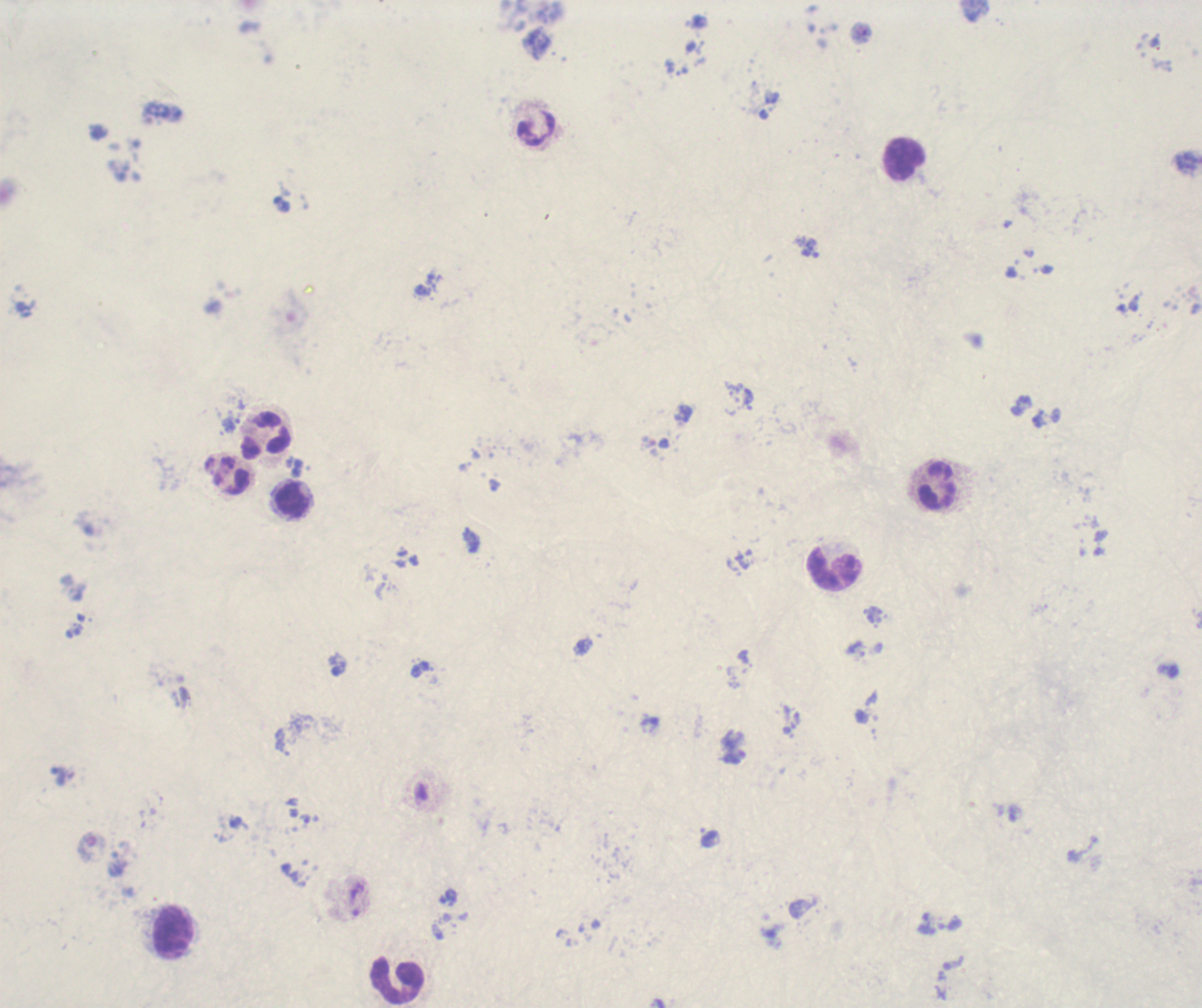
field_of_view: one from this slide
background_quality: unsatisfactory
trophozoite_locations: 'approximate centers as [x, y] in pixels: [811, 248]'
preparation: thick blood film
result: malaria parasites detected
context: previously used in a real diagnosis
stain: Romanowsky
leukocyte_locations: 'approximate centers as [x, y] in pixels: [537, 130], [905, 160], [267, 435], [938, 484], [293, 501], [834, 569], [175, 933], [399, 982]'
image_size: 1202×1008 pixels
magnification: 100x